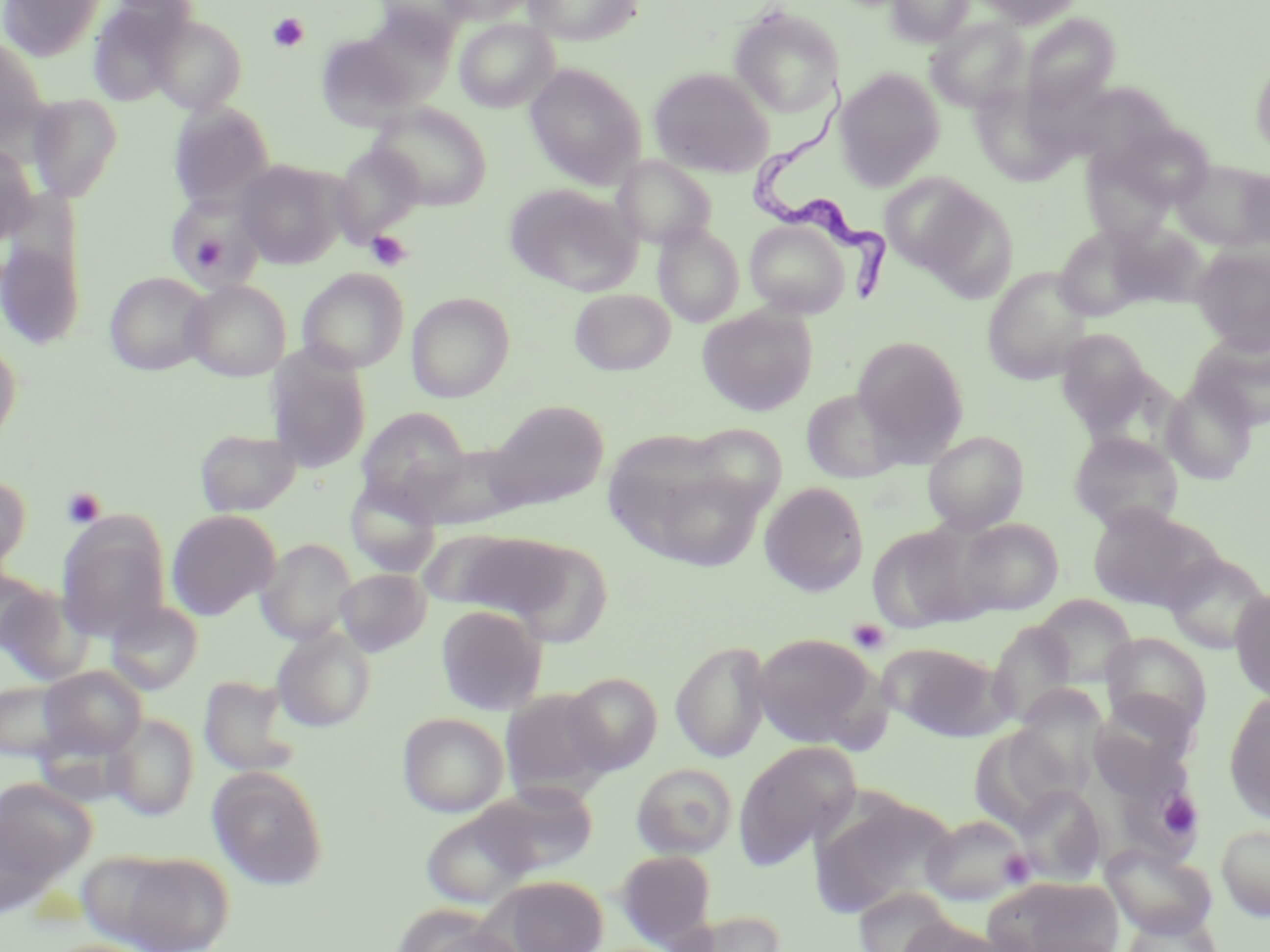

Summary:
  - Coordinate format: approximate bounding boxes as (x1,y1)-(x2,y2) corner pairs in pixels
  - Platelet locations: (268,13)-(309,53), (193,231)-(228,269), (366,231)-(412,270), (61,487)-(106,529), (848,618)-(890,655), (1156,791)-(1203,837), (998,850)-(1035,887)
  - Uninfected red blood cell locations: (0,0)-(105,61), (373,0)-(473,44), (439,0)-(536,25), (522,0)-(643,45), (886,0)-(974,47), (969,0)-(1084,28), (87,2)-(189,106), (728,6)-(844,118), (357,10)-(458,106), (1021,13)-(1120,114), (149,15)-(247,115), (926,17)-(1029,113), (455,18)-(558,113), (316,33)-(421,130), (0,34)-(50,148), (1250,57)-(1270,159), (525,64)-(647,189), (648,67)-(774,178), (835,69)-(946,190), (26,94)-(123,201), (168,102)-(276,211), (370,103)-(492,209), (1116,124)-(1214,209), (0,142)-(38,246), (330,142)-(427,246), (1082,150)-(1175,245), (613,155)-(717,251), (235,160)-(348,268), (1172,160)-(1270,251), (1238,167)-(1270,251), (879,173)-(992,275), (504,183)-(640,296), (915,190)-(1019,301), (166,196)-(263,292), (745,220)-(849,317), (1110,221)-(1207,309), (653,223)-(744,327), (1054,227)-(1148,321), (0,230)-(86,352), (1190,247)-(1270,353), (982,267)-(1095,384), (298,268)-(409,373), (104,272)-(213,376), (182,280)-(291,382), (296,280)-(514,381), (569,288)-(677,376), (406,292)-(515,401), (697,307)-(817,416), (1056,329)-(1157,436), (1188,332)-(1270,431), (851,335)-(969,461), (0,336)-(21,449), (267,346)-(371,473), (1162,379)-(1257,484), (800,389)-(908,484), (486,399)-(609,510), (356,408)-(471,510), (682,423)-(789,518), (194,428)-(302,517), (922,430)-(1029,534), (1069,432)-(1184,534), (611,439)-(772,573), (411,444)-(529,530), (0,474)-(31,578), (345,478)-(442,578), (759,481)-(869,596), (1087,502)-(1221,612), (167,509)-(281,620), (56,513)-(171,641), (954,518)-(1063,615), (867,522)-(988,633), (426,529)-(590,626), (255,538)-(357,644), (530,548)-(613,650), (1163,550)-(1269,654), (0,567)-(52,655), (335,568)-(430,656), (0,583)-(94,686), (1230,588)-(1270,704), (1033,595)-(1137,687), (105,600)-(203,694), (435,605)-(547,715), (988,621)-(1078,727), (271,627)-(376,732), (751,632)-(884,749), (1100,632)-(1212,736), (671,639)-(772,763), (879,643)-(1010,741), (38,666)-(147,760), (563,672)-(662,775), (199,675)-(301,778), (0,680)-(77,762), (501,689)-(613,799), (1224,692)-(1270,824), (1091,694)-(1194,795), (397,712)-(509,817), (105,713)-(199,820), (999,715)-(1094,814), (974,722)-(1068,834), (732,740)-(861,869), (631,763)-(737,860), (208,767)-(329,890), (0,777)-(96,885), (471,783)-(598,877), (1012,785)-(1106,884), (809,792)-(956,918), (420,805)-(538,908), (0,812)-(59,919), (921,813)-(1034,906), (1216,823)-(1270,921), (1102,843)-(1217,939), (106,850)-(234,952), (615,850)-(717,947), (983,875)-(1122,952), (491,876)-(609,952), (853,886)-(959,951), (398,909)-(524,952), (667,911)-(787,952), (1118,912)-(1226,952), (898,917)-(1021,952), (1017,934)-(1126,952)
  - Trypanosoma brucei locations: (755,78)-(895,306)
  - Slide-level diagnosis: Trypanosoma brucei
  - Preparation: thin blood film
  - Image size: 1270×952 pixels
  - Modality: light microscopy
  - Stain: May-Grünwald-Giemsa
  - Magnification: 1000x
  - Field of view: single